Report the malaria status of this cell.
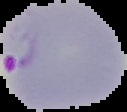

It is parasitized.

{
  "image_size": "127×112 pixels",
  "image_type": "segmented cell region with the area outside set to black",
  "preparation": "thin blood smear"
}